Report the malaria status of this cell.
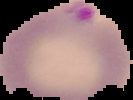
Parasitized.

image size = 133×100 pixels
image type = cell region segmented out of the field of view; surrounding area masked to black
preparation = thin blood smear